Report the malaria status of this cell.
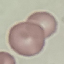
It is uninfected.

Summary:
  - Stain: Giemsa
  - Image type: automatically extracted cell patch, resized to 64 × 64 pixels
  - Preparation: thin blood smear
  - Capture: smartphone through the microscope eyepiece